Assess this cell for malaria.
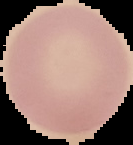

It is uninfected.

preparation: thin blood smear
image_type: segmented cell region on a black background
image_size: 133×145 pixels